Name the parasite shown.
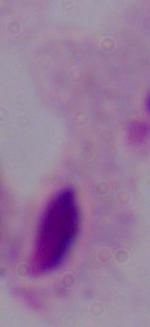
A trichomonad.

Summary:
  - Magnification: 1000x
  - Modality: micrograph